Give a bounding box for every leukocyte visible.
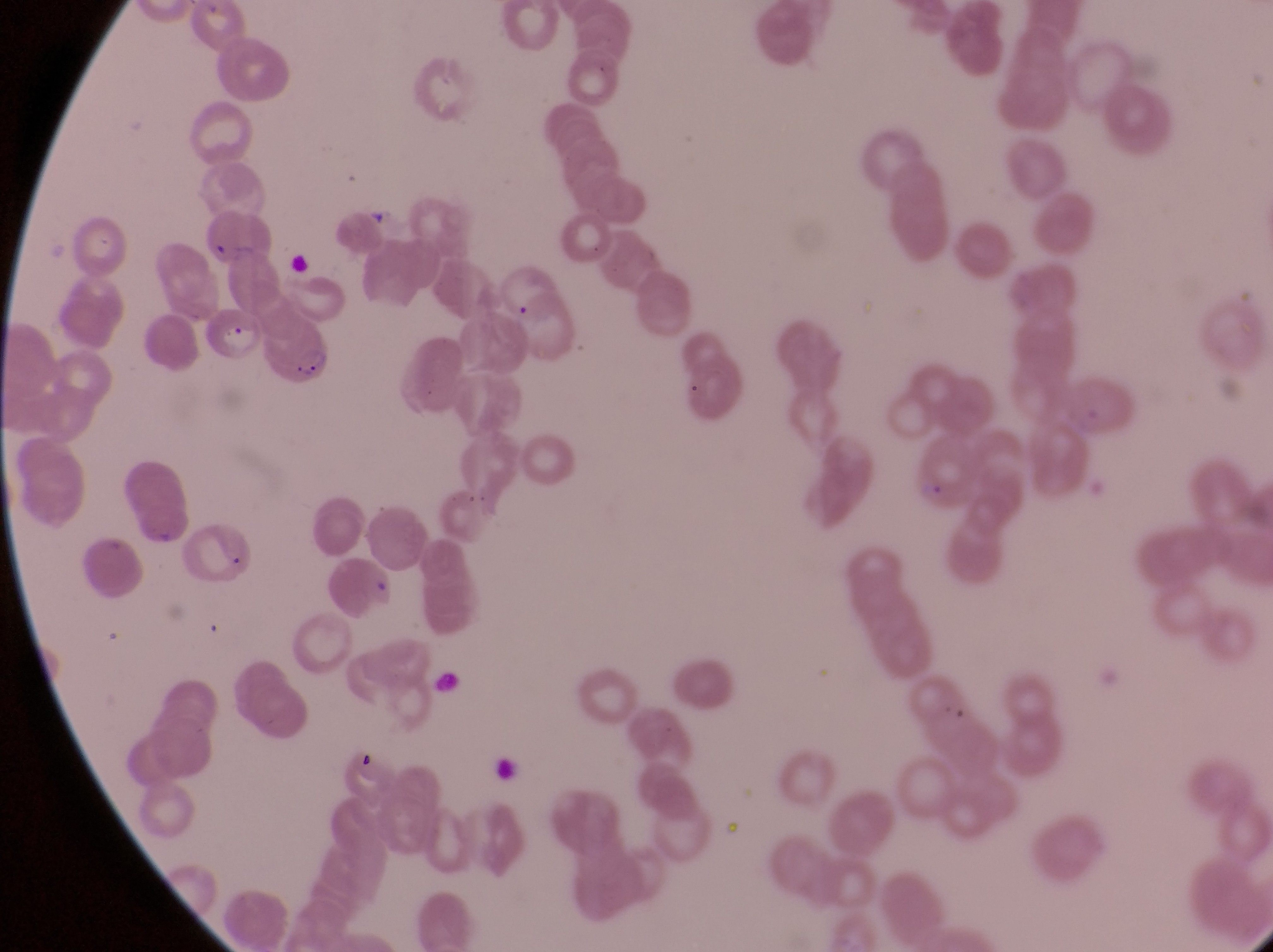

No leukocytes observed.

Approximate bounding boxes as {left, top, right, bottom} in pixels. Parasitised red blood cell locations: {206, 306, 261, 371}, {259, 318, 333, 390}. Artifact (platelet-like body, stain precipitate, or debris) locations: {430, 665, 467, 702}, {345, 746, 382, 779}. Photographed through the eyepiece of an Olympus CX-23 microscope with a smartphone camera. Thin blood smear. Single field of view. Collected in Uganda. Image is 1273×952 pixels. At a magnification of 1000x.